Assess this cell for malaria.
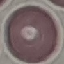

It is uninfected.

Summary:
  - Preparation: thin blood smear
  - Stain: Giemsa
  - Capture: smartphone camera at the microscope eyepiece
  - Image type: automatically extracted cell patch, resized to 64 × 64 pixels